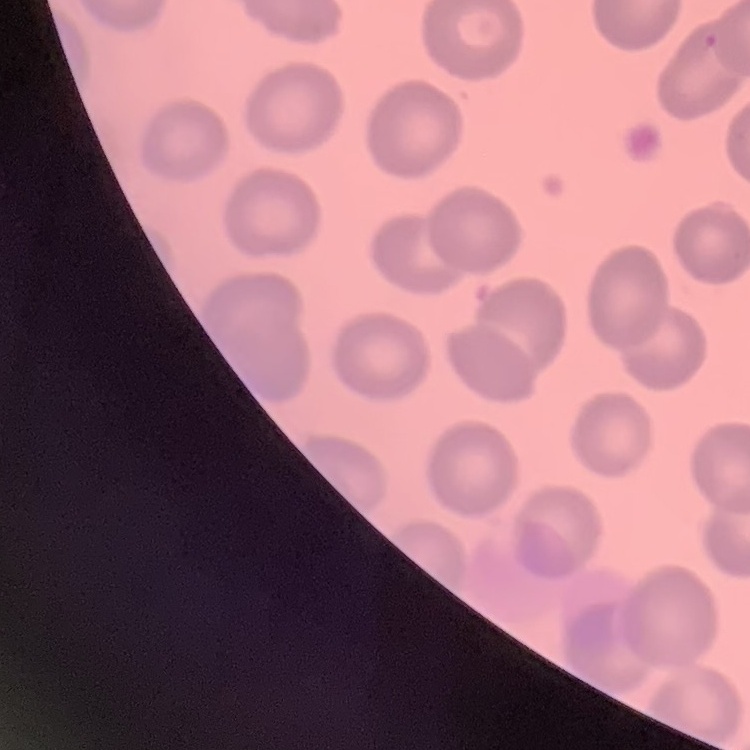
Summary:
  - Erythrocyte morphology: no rouleaux formation
  - Preparation: thin blood smear
  - Image type: one tile cut from a larger photomicrograph
  - Stain: Field's or Giemsa